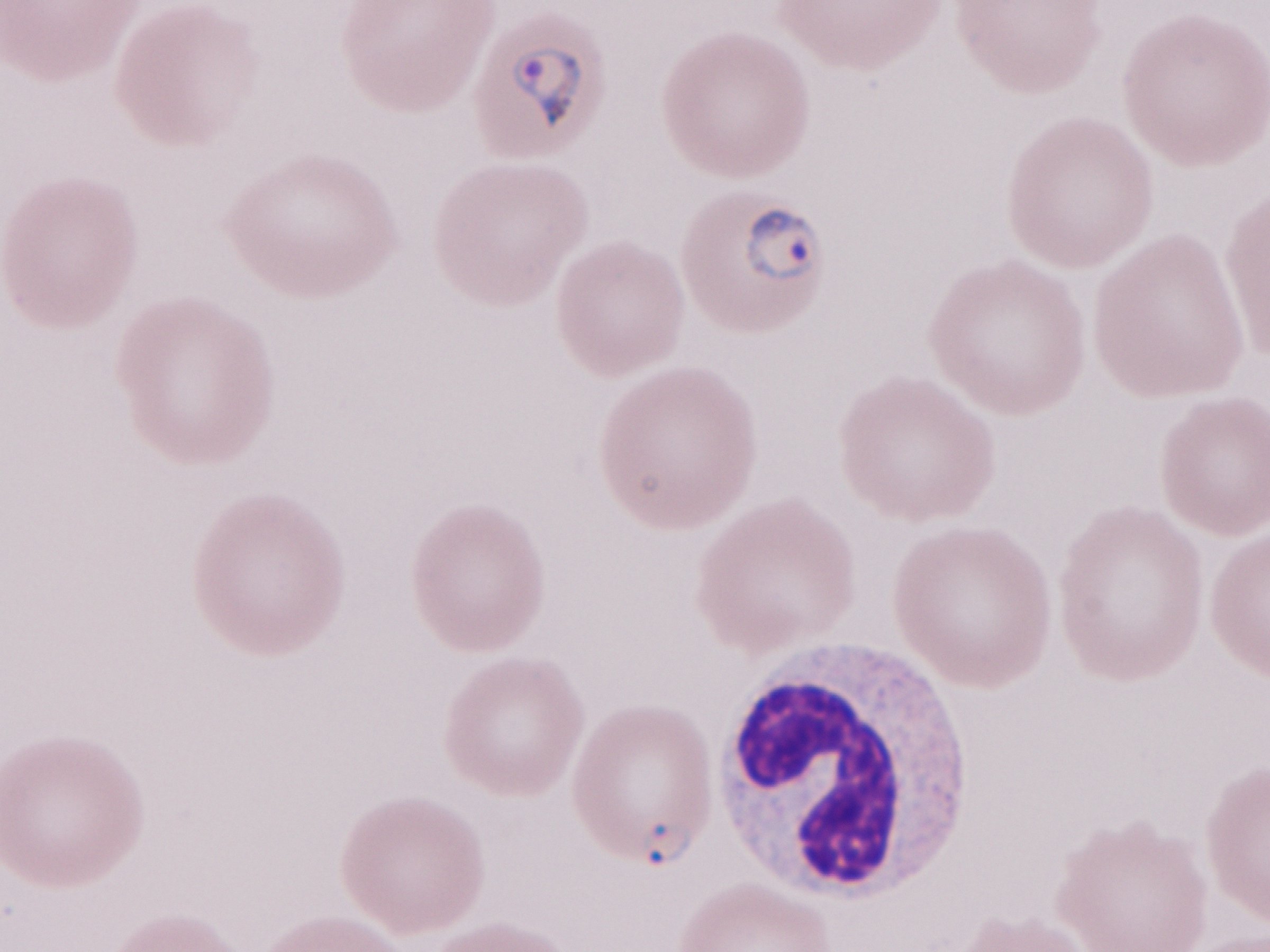
One field of this slide. Patient-level malaria diagnosis: positive. Image is 1270×952 pixels. May-Grünwald-Giemsa (MGG) stain. Olympus BX43 microscope, Olympus DP73 camera. Magnification: 1,000x. Thin peripheral-blood smear.